Locate every malaria parasite.
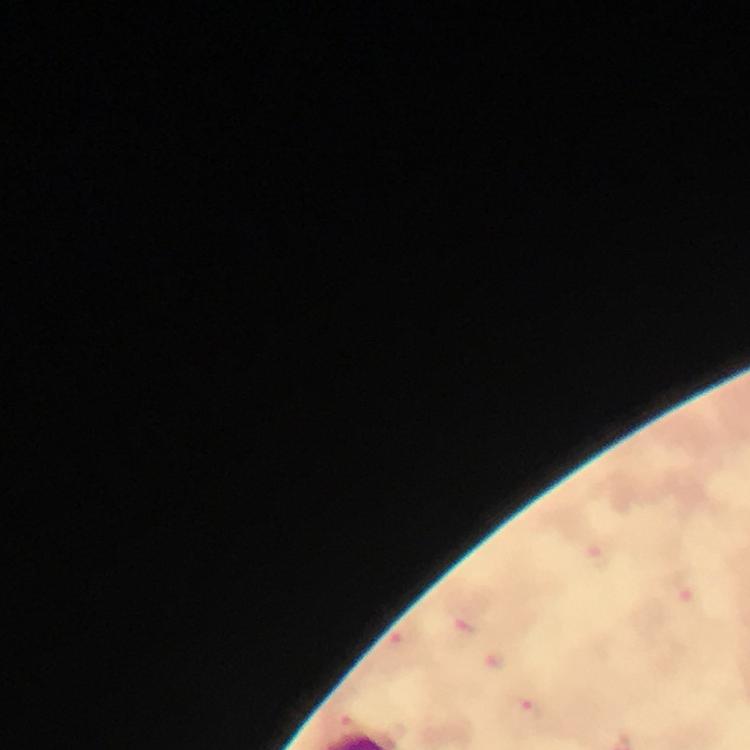

Approximate object centers, in pixels from the top-left corner.
Malaria parasites: (x=464, y=632), (x=398, y=644), (x=492, y=664), (x=528, y=707).

Giemsa stain. Image is 750×750 pixels. Thick smear. From a malaria diagnostic workup. Photographed with a smartphone mounted on the microscope. At 100x magnification. Immersion oil applied. A crop from one field of view.